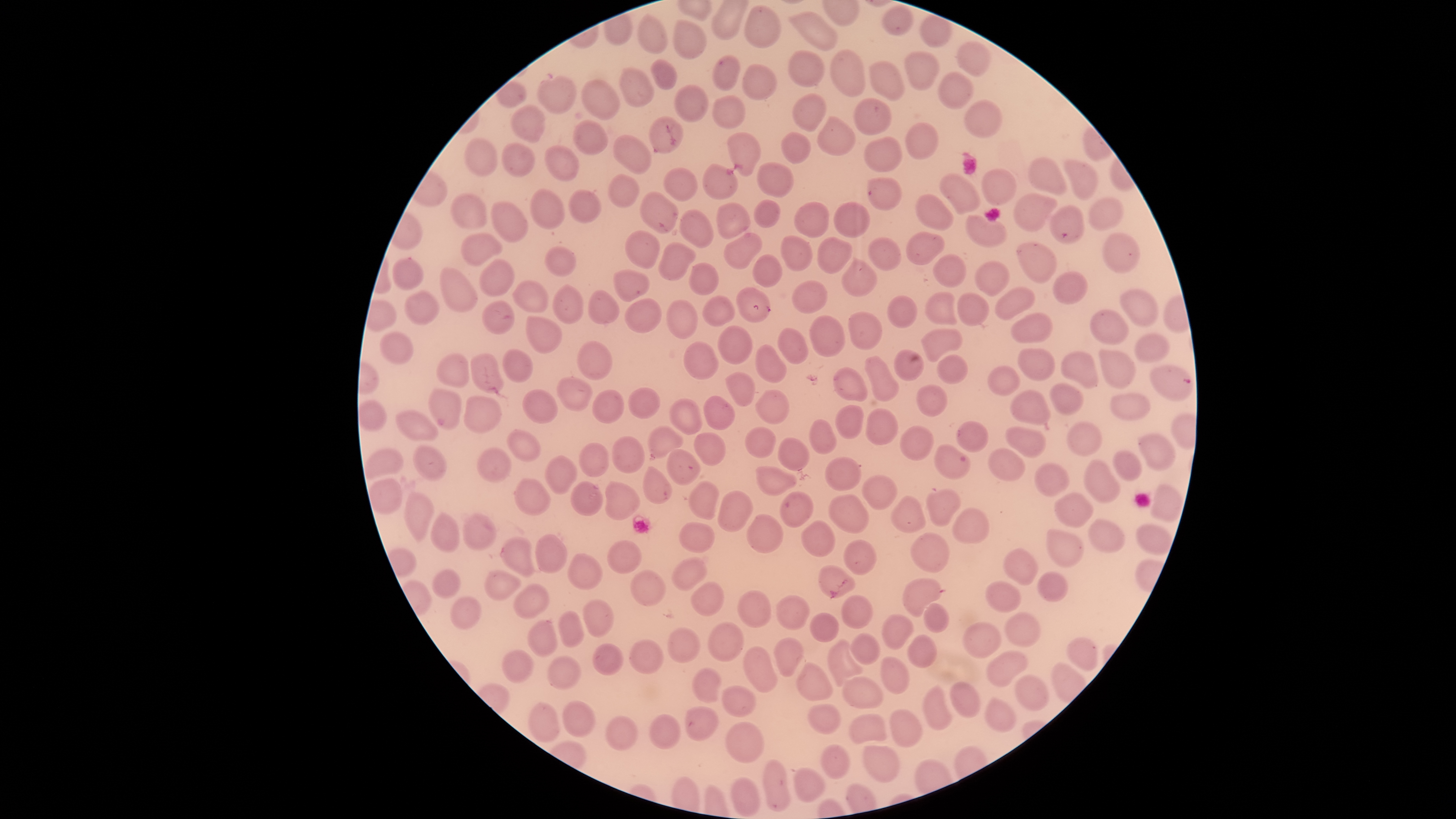

Approximate bounding boxes as {left, top, right, bottom} in pixels.
Summary:
  - Uninfected red blood cells: {745, 6, 779, 47}, {882, 8, 913, 35}, {790, 12, 835, 50}, {639, 16, 667, 54}, {921, 16, 949, 47}, {675, 20, 705, 59}, {956, 43, 988, 77}, {788, 50, 824, 87}, {830, 50, 866, 97}, {906, 53, 939, 90}, {714, 56, 740, 91}, {651, 61, 676, 89}, {867, 62, 904, 100}, {743, 65, 776, 99}, {620, 67, 653, 106}, {937, 74, 972, 108}, {537, 76, 576, 113}, {581, 79, 619, 119}, {674, 86, 708, 122}, {794, 94, 826, 132}, {713, 96, 744, 129}, {854, 99, 891, 134}, {965, 101, 1001, 139}, {511, 106, 545, 143}, {649, 116, 683, 153}, {816, 116, 855, 158}, {574, 120, 608, 155}, {906, 121, 939, 160}, {728, 132, 760, 178}, {782, 132, 810, 163}, {614, 135, 651, 174}, {464, 138, 498, 175}, {864, 138, 901, 173}, {502, 143, 534, 177}, {544, 146, 580, 182}, {1029, 158, 1068, 195}, {1065, 159, 1096, 200}, {758, 163, 792, 197}, {702, 164, 737, 198}, {664, 167, 696, 200}, {981, 169, 1015, 206}, {608, 174, 639, 207}, {940, 174, 979, 214}, {866, 176, 901, 210}, {531, 190, 565, 228}, {567, 190, 602, 223}, {640, 190, 678, 234}, {1014, 193, 1056, 232}, {451, 194, 486, 228}, {916, 194, 953, 230}, {1087, 198, 1123, 232}, {753, 200, 779, 227}, {794, 202, 828, 239}, {834, 202, 869, 236}, {492, 203, 528, 243}, {716, 204, 748, 237}, {1051, 206, 1087, 243}, {678, 209, 714, 248}, {966, 214, 1006, 246}, {625, 231, 659, 268}, {906, 232, 943, 265}, {461, 233, 501, 265}, {1103, 233, 1140, 273}, {723, 234, 762, 271}, {780, 236, 812, 271}, {869, 237, 902, 271}, {817, 238, 850, 274}, {659, 242, 694, 281}, {1017, 243, 1055, 283}, {544, 247, 576, 276}, {933, 254, 966, 287}, {752, 255, 782, 287}, {392, 259, 423, 290}, {841, 259, 876, 296}, {479, 260, 514, 296}, {975, 262, 1009, 296}, {688, 263, 717, 294}, {440, 266, 478, 313}, {614, 271, 648, 301}, {1052, 271, 1087, 304}, {792, 280, 828, 313}, {512, 281, 548, 313}, {553, 284, 585, 325}, {996, 287, 1035, 321}, {735, 288, 770, 322}, {1121, 288, 1158, 328}, {587, 290, 618, 324}, {405, 292, 439, 325}, {926, 292, 959, 326}, {957, 293, 988, 327}, {887, 295, 917, 327}, {701, 296, 735, 327}, {624, 298, 661, 332}, {665, 299, 698, 339}, {482, 300, 514, 333}, {1091, 310, 1129, 345}, {851, 311, 880, 350}, {1011, 314, 1053, 343}, {809, 315, 845, 358}, {525, 316, 562, 353}, {717, 325, 752, 364}, {778, 327, 808, 364}, {920, 327, 963, 361}, {379, 333, 413, 363}, {1134, 335, 1169, 363}, {577, 342, 611, 380}, {684, 342, 719, 381}, {755, 345, 786, 384}, {1018, 347, 1055, 380}, {1060, 349, 1098, 388}, {1100, 349, 1136, 388}, {502, 350, 533, 382}, {894, 350, 923, 382}, {436, 354, 468, 388}, {471, 354, 503, 394}, {937, 355, 967, 384}, {864, 357, 898, 401}, {988, 366, 1019, 394}, {833, 367, 868, 401}, {726, 372, 755, 406}, {557, 378, 593, 412}, {1048, 383, 1085, 416}, {916, 384, 948, 417}, {628, 387, 660, 418}, {428, 389, 462, 428}, {755, 389, 790, 424}, {521, 390, 558, 424}, {592, 390, 624, 424}, {1011, 390, 1052, 425}, {1111, 394, 1151, 419}, {703, 395, 735, 428}, {464, 397, 501, 434}, {669, 400, 703, 434}, {358, 402, 385, 431}, {836, 406, 863, 440}, {865, 409, 896, 445}, {397, 411, 437, 441}, {810, 419, 837, 454}, {956, 421, 988, 452}, {1068, 422, 1099, 455}, {648, 425, 683, 458}, {900, 426, 933, 460}, {1005, 426, 1046, 458}, {745, 427, 776, 458}, {508, 430, 541, 461}, {693, 432, 725, 466}, {1139, 435, 1174, 469}, {612, 436, 645, 473}, {778, 438, 808, 470}, {578, 441, 608, 476}, {414, 445, 445, 479}, {936, 445, 970, 481}, {364, 447, 403, 479}, {666, 448, 700, 485}, {477, 449, 511, 482}, {988, 449, 1024, 481}, {1113, 451, 1141, 481}, {546, 456, 576, 494}, {825, 458, 861, 492}, {1084, 459, 1120, 502}, {1035, 463, 1068, 496}, {756, 464, 798, 496}, {642, 466, 673, 504}, {862, 475, 896, 509}, {369, 479, 402, 513}, {515, 479, 549, 515}, {570, 481, 601, 516}, {689, 481, 719, 519}, {605, 482, 639, 519}, {1151, 486, 1181, 522}, {925, 489, 960, 527}, {718, 491, 755, 531}, {404, 493, 434, 543}, {780, 493, 812, 527}, {1054, 493, 1093, 528}, {830, 495, 869, 533}, {891, 495, 928, 532}, {953, 508, 989, 543}, {430, 514, 459, 553}, {747, 514, 785, 554}, {463, 515, 495, 549}, {1088, 519, 1124, 552}, {800, 520, 835, 557}, {677, 522, 715, 553}, {1136, 524, 1172, 554}, {1046, 529, 1084, 567}, {910, 533, 949, 573}, {533, 535, 566, 574}, {501, 538, 536, 575}, {844, 539, 876, 576}, {607, 540, 641, 573}, {1003, 550, 1039, 585}, {567, 554, 603, 589}, {671, 557, 708, 591}, {818, 565, 855, 600}, {432, 570, 459, 598}, {484, 570, 521, 601}, {631, 571, 665, 606}, {1037, 572, 1068, 602}, {903, 579, 942, 618}, {985, 581, 1020, 612}, {691, 583, 724, 618}, {514, 585, 548, 618}, {737, 591, 772, 629}, {776, 595, 809, 631}, {840, 596, 871, 629}, {451, 597, 481, 630}, {582, 599, 613, 639}, {924, 604, 948, 633}, {558, 611, 585, 648}, {809, 613, 838, 642}, {1005, 613, 1041, 648}, {881, 614, 913, 650}, {530, 620, 557, 656}, {962, 622, 1000, 658}, {708, 623, 743, 662}, {667, 628, 700, 664}, {850, 634, 880, 664}, {907, 634, 937, 669}, {774, 637, 804, 679}, {1067, 638, 1097, 671}, {629, 640, 662, 673}, {828, 640, 864, 688}, {593, 644, 623, 674}, {744, 646, 777, 693}, {502, 650, 534, 684}, {986, 652, 1027, 686}, {880, 655, 909, 695}, {548, 656, 580, 689}, {797, 662, 834, 701}, {691, 668, 721, 704}, {1016, 676, 1049, 710}, {842, 677, 882, 708}, {950, 682, 979, 717}, {922, 685, 953, 731}, {723, 686, 756, 717}, {984, 699, 1016, 733}, {529, 702, 559, 741}, {563, 703, 595, 736}, {807, 704, 841, 734}, {685, 706, 718, 741}, {888, 708, 921, 747}, {849, 714, 887, 743}, {650, 715, 680, 750}, {605, 716, 637, 751}, {725, 723, 764, 763}, {821, 745, 852, 779}, {862, 745, 900, 783}, {763, 760, 789, 811}, {794, 768, 825, 804}, {731, 778, 758, 817}
  - Parasitized red blood cells: {1150, 366, 1194, 403}
  - Preparation: thin smear of blood
  - Species: Plasmodium falciparum
  - Presence: malaria parasites identified
  - Visible region: circular
  - Stain: Giemsa
  - Field of view: single
  - Image size: 1456×819 pixels
  - Capture: smartphone photograph through the microscope eyepiece